State the blood parasite species.
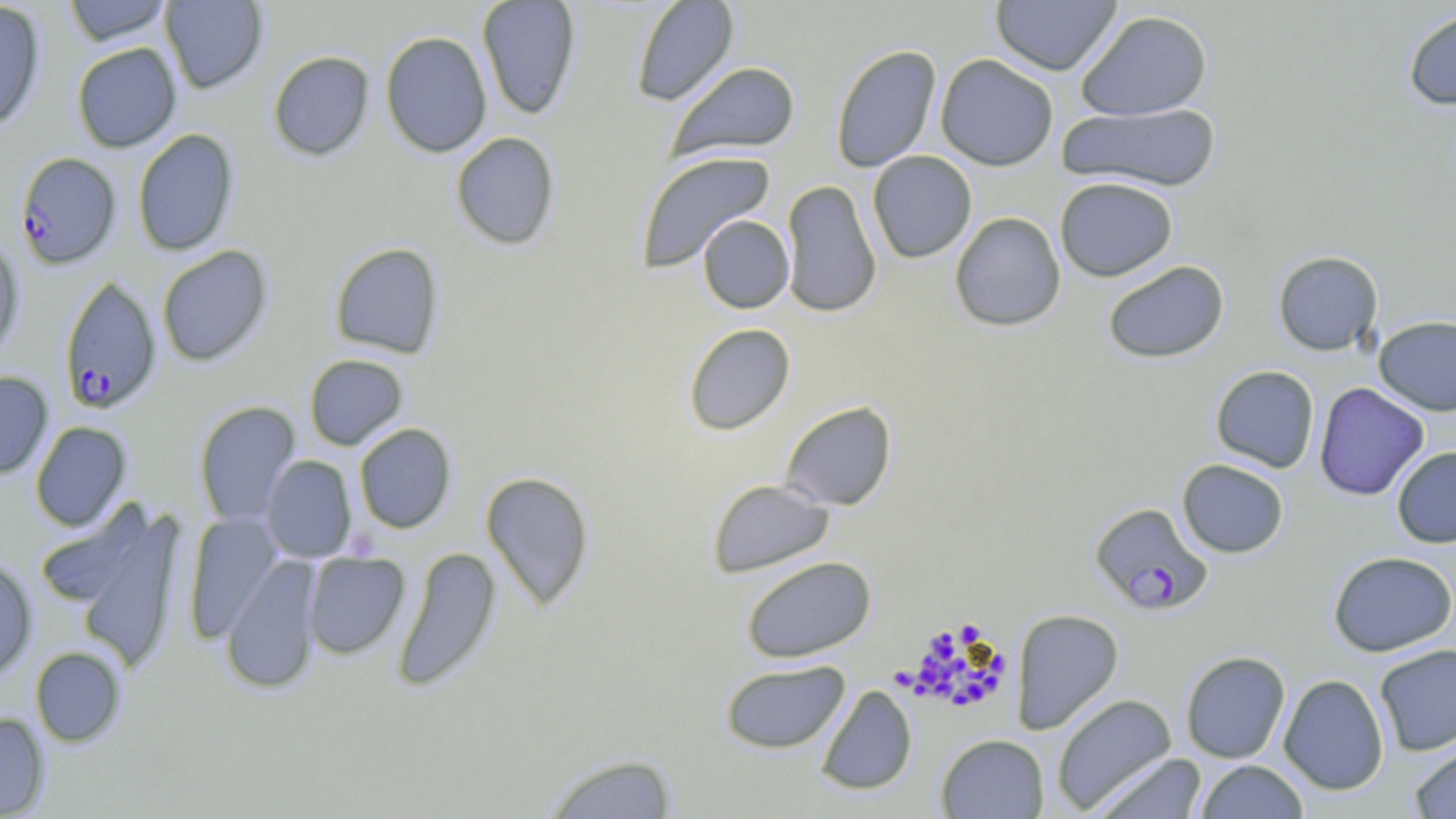

Plasmodium falciparum.

Approximate bounding boxes as (x1, y1, x2, y2) in pixels. Plasmodium falciparum-infected red blood cell locations: (15, 152, 121, 270), (59, 274, 163, 414), (1089, 502, 1213, 615). Uninfected red blood cell locations: (62, 0, 173, 46), (160, 0, 268, 94), (477, 0, 581, 119), (630, 0, 739, 107), (991, 0, 1122, 75), (0, 1, 46, 132), (1402, 6, 1456, 111), (1075, 9, 1214, 122), (380, 31, 492, 158), (71, 42, 182, 152), (830, 44, 942, 173), (268, 50, 374, 161), (935, 54, 1059, 171), (667, 61, 801, 161), (1058, 102, 1222, 193), (131, 128, 240, 256), (450, 132, 561, 251), (635, 151, 776, 274), (868, 151, 977, 263), (1054, 177, 1178, 282), (780, 180, 881, 318), (950, 212, 1066, 332), (697, 214, 795, 313), (0, 237, 24, 361), (329, 242, 444, 359), (156, 245, 274, 367), (1272, 250, 1384, 356), (1102, 260, 1230, 364), (1373, 315, 1456, 416), (683, 322, 796, 435), (304, 354, 409, 450), (1210, 365, 1320, 473), (0, 371, 53, 479), (1314, 382, 1429, 500), (193, 401, 301, 527), (779, 401, 897, 511), (30, 421, 132, 532), (353, 423, 456, 534), (1391, 446, 1456, 548), (261, 455, 357, 564), (1177, 458, 1289, 558), (480, 470, 596, 611), (707, 479, 835, 578), (52, 499, 189, 673), (35, 501, 154, 611), (183, 512, 283, 644), (392, 546, 501, 694), (1327, 550, 1456, 657), (302, 551, 410, 659), (0, 556, 37, 682), (221, 556, 322, 695), (741, 556, 877, 663), (1010, 608, 1124, 734), (1374, 644, 1456, 756), (30, 646, 126, 747), (1180, 650, 1291, 764), (719, 660, 850, 754), (1279, 674, 1389, 795), (815, 684, 918, 795), (1051, 693, 1177, 814), (0, 712, 50, 817), (935, 733, 1049, 818), (1408, 741, 1456, 818), (540, 752, 680, 819), (1090, 752, 1208, 819), (1195, 760, 1309, 819). Thin blood film. Optical microscopy. May-Grünwald-Giemsa-stained preparation. Image is 1456×819 pixels. Single field of view. Captured at 1000x magnification.